Report the malaria status of this cell.
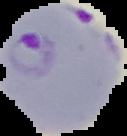

Parasitized.

Summary:
  - Image size: 127×136 pixels
  - Preparation: thin blood smear
  - Image type: segmented cell region on a black background